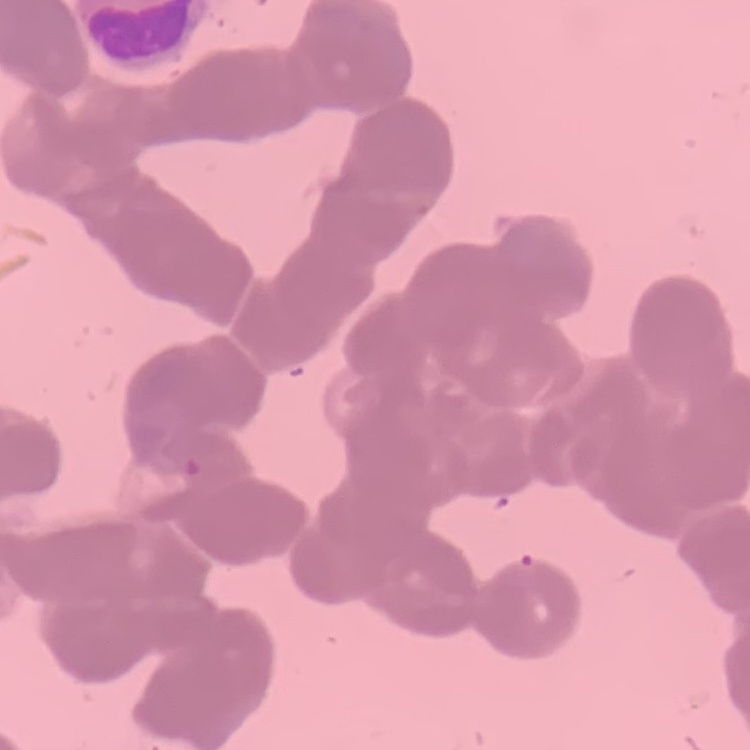
erythrocyte_morphology: rouleaux formation
stain: Field's or Giemsa
preparation: thin blood smear
image_type: one tile cut from a larger photomicrograph